Give the extent of all uninfected red blood cells.
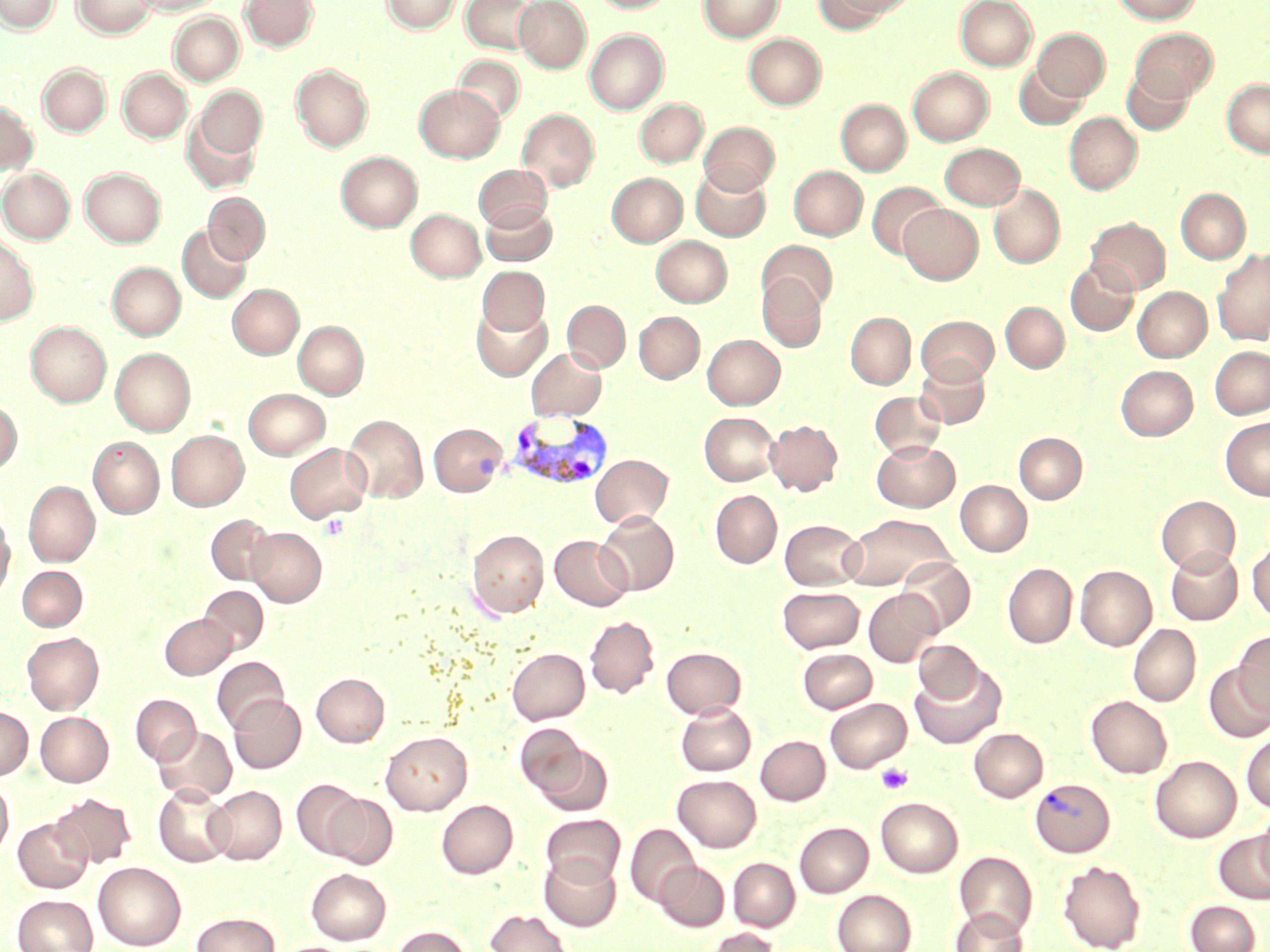
Approximate bounding boxes as [x1, y1, x2, y2] in pixels.
Uninfected red blood cells: [0, 0, 61, 33], [72, 0, 157, 38], [137, 0, 221, 15], [241, 0, 317, 51], [382, 0, 459, 33], [461, 0, 540, 54], [514, 0, 591, 72], [588, 0, 675, 13], [699, 0, 783, 42], [813, 0, 901, 31], [955, 0, 1037, 70], [1112, 0, 1202, 24], [169, 13, 244, 85], [1033, 28, 1110, 101], [1130, 28, 1218, 102], [585, 29, 668, 113], [744, 33, 826, 109], [453, 55, 524, 124], [1014, 63, 1088, 129], [38, 64, 111, 136], [291, 64, 373, 152], [908, 67, 993, 145], [1122, 67, 1194, 134], [118, 68, 192, 142], [1222, 79, 1270, 157], [414, 84, 504, 161], [194, 86, 267, 160], [635, 98, 708, 167], [836, 99, 911, 175], [0, 101, 37, 174], [517, 108, 599, 192], [1064, 112, 1142, 195], [181, 114, 261, 194], [699, 122, 779, 195], [940, 143, 1024, 210], [337, 151, 422, 232], [473, 165, 552, 231], [789, 166, 867, 240], [80, 167, 165, 247], [691, 167, 771, 241], [0, 168, 75, 243], [607, 173, 687, 247], [867, 181, 945, 259], [989, 184, 1065, 268], [1177, 188, 1250, 264], [203, 193, 269, 264], [481, 203, 556, 266], [899, 204, 983, 284], [406, 209, 485, 281], [1086, 218, 1170, 293], [178, 225, 251, 303], [0, 236, 39, 326], [651, 236, 732, 306], [758, 241, 838, 313], [1213, 248, 1270, 346], [1065, 259, 1138, 336], [108, 262, 185, 340], [477, 266, 549, 336], [757, 274, 827, 352], [228, 284, 303, 359], [1133, 287, 1211, 361], [562, 300, 630, 372], [1001, 302, 1069, 372], [472, 304, 552, 381], [634, 311, 704, 383], [846, 312, 915, 389], [916, 315, 999, 385], [293, 320, 368, 399], [26, 322, 111, 406], [702, 334, 785, 409], [1210, 346, 1270, 419], [111, 348, 195, 436], [527, 349, 607, 420], [915, 356, 990, 429], [1116, 365, 1197, 440], [244, 388, 329, 459], [869, 391, 946, 459], [0, 401, 21, 474], [700, 412, 780, 485], [343, 414, 427, 502], [1220, 417, 1270, 500], [766, 420, 842, 495], [429, 423, 507, 495], [167, 430, 248, 510], [1014, 433, 1087, 503], [89, 437, 163, 518], [872, 440, 960, 512], [285, 443, 371, 523], [591, 454, 673, 528], [956, 480, 1032, 556], [24, 481, 100, 567], [710, 490, 782, 568], [1156, 496, 1240, 573], [595, 511, 679, 596], [841, 513, 956, 591], [206, 514, 279, 584], [0, 517, 14, 603], [781, 519, 865, 590], [248, 528, 326, 606], [467, 530, 548, 617], [551, 536, 632, 611], [1247, 543, 1270, 623], [1166, 546, 1243, 625], [896, 556, 976, 634], [1003, 563, 1077, 648], [1075, 565, 1156, 651], [17, 566, 87, 631], [199, 586, 268, 654], [778, 587, 864, 653], [863, 589, 942, 667], [160, 614, 235, 679], [585, 616, 658, 698], [1129, 624, 1200, 706], [1233, 631, 1270, 717], [22, 632, 104, 714], [913, 640, 985, 704], [662, 647, 746, 718], [508, 648, 589, 723], [798, 649, 877, 713], [212, 657, 288, 733], [1203, 662, 1270, 743], [910, 663, 1006, 749], [312, 673, 389, 747], [131, 694, 201, 765], [229, 695, 305, 773], [1087, 696, 1172, 778], [825, 698, 911, 772], [676, 703, 756, 775], [0, 708, 33, 779], [35, 712, 113, 786], [515, 723, 590, 800], [153, 726, 236, 802], [970, 728, 1047, 802], [381, 732, 471, 815], [1241, 732, 1270, 812], [756, 736, 830, 805], [532, 743, 613, 816], [1151, 756, 1240, 842], [673, 775, 761, 851], [291, 779, 367, 859], [0, 780, 13, 858], [154, 785, 235, 867], [205, 786, 286, 864], [51, 793, 136, 868], [323, 793, 397, 869], [876, 797, 962, 877], [437, 800, 518, 878], [1256, 811, 1270, 889], [541, 814, 624, 887], [13, 818, 92, 893], [795, 823, 873, 897], [625, 824, 700, 908], [1214, 831, 1270, 904], [954, 851, 1037, 937], [539, 854, 620, 931], [729, 858, 800, 931], [655, 861, 729, 931], [1058, 861, 1146, 952], [93, 862, 186, 951], [306, 868, 391, 944], [832, 889, 916, 952], [12, 894, 98, 952], [1185, 901, 1260, 952], [951, 908, 1028, 952], [485, 910, 571, 951], [191, 913, 280, 952], [391, 926, 470, 952], [702, 928, 781, 952].

{
  "slide_level_diagnosis": "Plasmodium vivax",
  "field_of_view": "single",
  "stain": "May-Grünwald-Giemsa",
  "preparation": "thin blood film",
  "platelet_locations": "approximate bounding boxes as [x1, y1, x2, y2] in pixels: [320, 513, 349, 540], [876, 763, 913, 794]",
  "magnification": "1000x",
  "image_size": "1270×952 pixels",
  "plasmodium_vivax_infected_red_blood_cell_locations": "approximate bounding boxes as [x1, y1, x2, y2] in pixels: [507, 412, 613, 492], [1030, 778, 1115, 857]",
  "modality": "optical microscopy"
}